State which parasite is depicted.
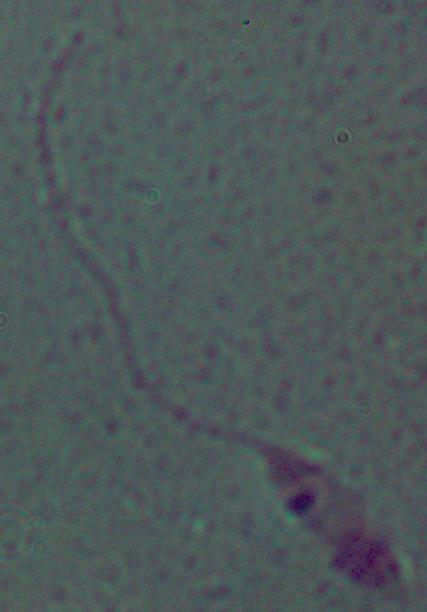

This is Leishmania.

Micrograph. Captured at 1000x magnification.